Classify this cell by malaria status.
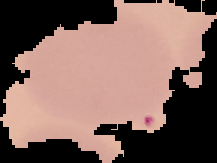
It is uninfected.

Summary:
  - Image size: 217×163 pixels
  - Image type: segmented cell region on a black background
  - Preparation: thin blood smear